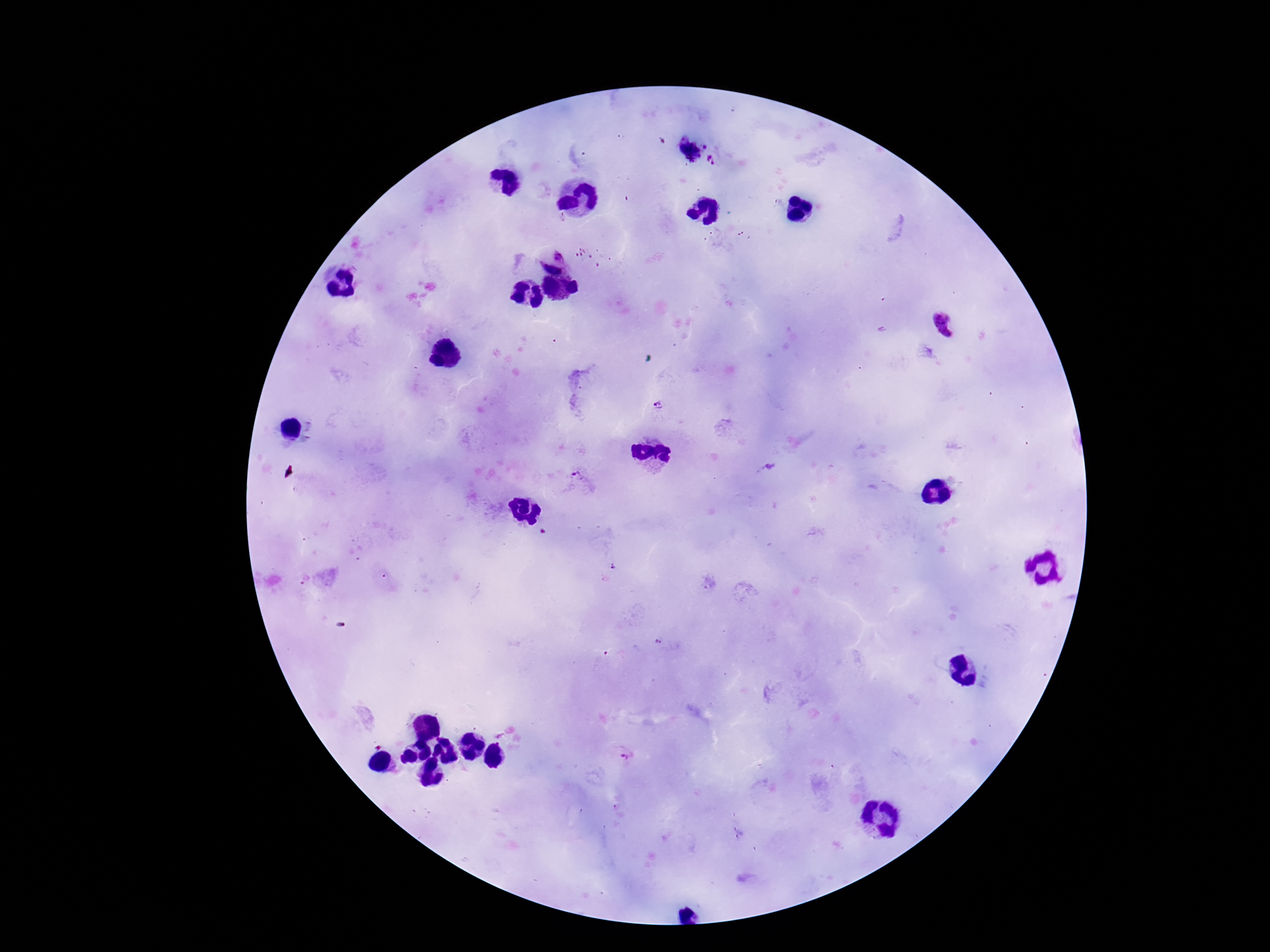
Approximate centers as [x, y] in pixels.
Summary:
  - Plasmodium parasite locations: [706, 145], [688, 151], [712, 161], [559, 253], [596, 255], [553, 268], [945, 325], [661, 405], [581, 479], [658, 642], [627, 754]
  - Field of view: single
  - Capture: smartphone camera through the microscope eyepiece
  - Stain: Giemsa
  - Patient malaria status: infected
  - Preparation: thick blood film
  - Image size: 1270×952 pixels
  - Magnification: 100x